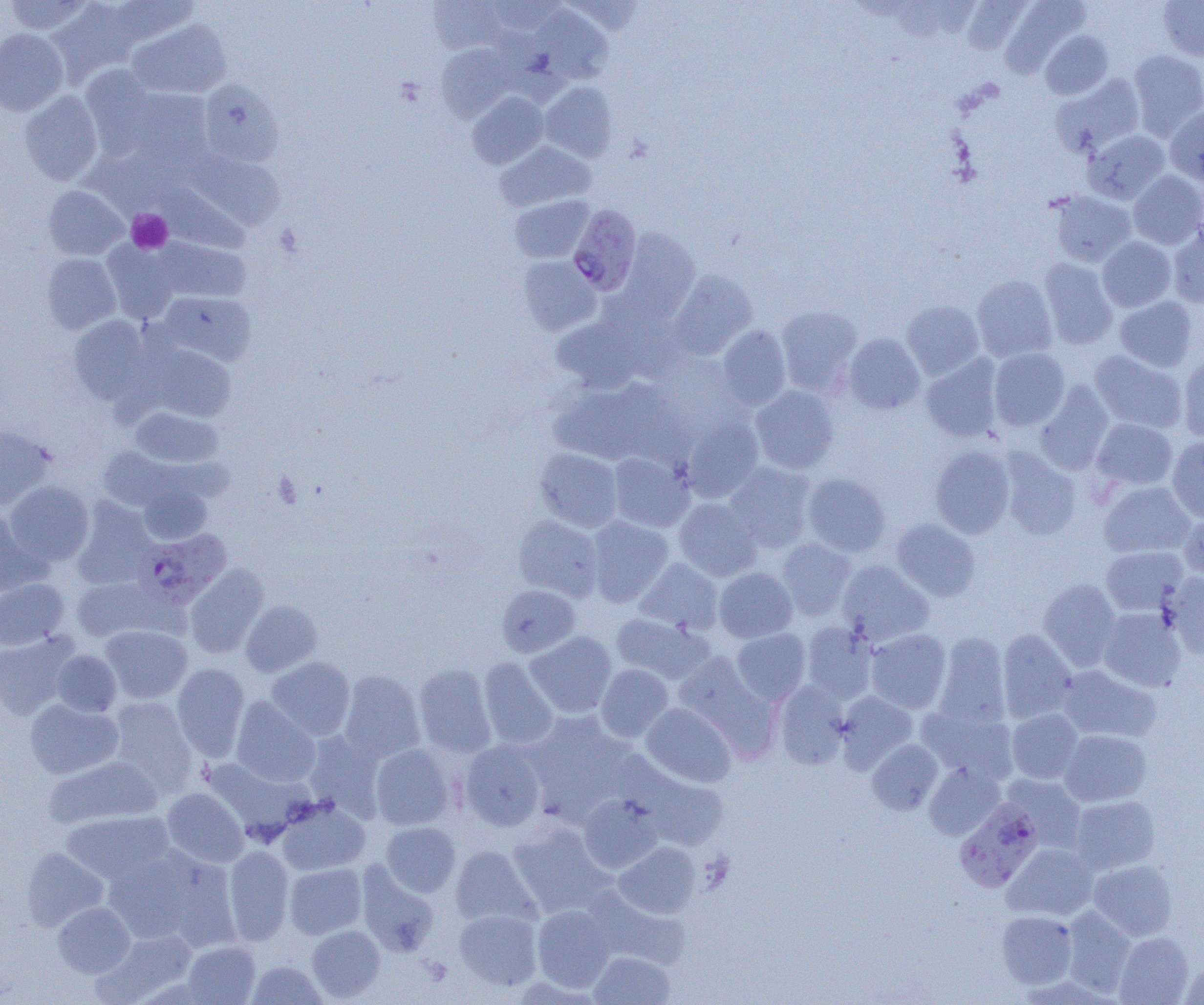
slide-level diagnosis = Plasmodium falciparum
image size = 1204×1005 pixels
platelet locations = approximate bounding boxes as (x1, y1, x2, y2) in pixels: (127, 209, 172, 253)
uninfected red blood cell locations = approximate bounding boxes as (x1, y1, x2, y2) in pixels: (3, 0, 93, 36), (108, 0, 200, 49), (428, 0, 508, 54), (484, 0, 566, 36), (960, 0, 1032, 56), (46, 1, 138, 84), (999, 1, 1090, 77), (1157, 1, 1204, 61), (531, 5, 613, 86), (126, 19, 231, 99), (0, 28, 68, 115), (1040, 31, 1114, 100), (435, 43, 515, 121), (1128, 49, 1204, 139), (81, 66, 159, 153), (1050, 74, 1145, 157), (197, 80, 284, 167), (539, 81, 618, 162), (123, 87, 215, 172), (20, 90, 103, 186), (467, 91, 548, 169), (1165, 105, 1204, 185), (1083, 129, 1170, 204), (495, 140, 595, 212), (183, 150, 285, 229), (1128, 170, 1204, 249), (159, 184, 249, 253), (43, 185, 129, 260), (1047, 190, 1136, 267), (510, 195, 594, 264), (1168, 224, 1204, 308), (612, 228, 700, 325), (152, 237, 250, 304), (1097, 237, 1176, 311), (102, 240, 180, 323), (42, 253, 122, 334), (518, 255, 601, 336), (1039, 258, 1118, 350), (666, 270, 757, 360), (972, 275, 1057, 362), (156, 291, 257, 367), (1115, 296, 1199, 372), (900, 299, 984, 380), (777, 305, 862, 395), (68, 315, 155, 405), (552, 317, 644, 393), (716, 325, 791, 411), (842, 333, 925, 415), (145, 345, 236, 422), (989, 348, 1070, 431), (1089, 350, 1187, 433), (1178, 353, 1204, 444), (920, 354, 1003, 442), (548, 379, 663, 466), (1033, 381, 1114, 475), (750, 386, 839, 475), (130, 406, 223, 468), (681, 415, 763, 502), (1091, 418, 1178, 492), (0, 424, 55, 509), (1167, 437, 1204, 521), (929, 445, 1015, 538), (97, 447, 181, 512), (534, 448, 622, 532), (998, 449, 1081, 540), (607, 452, 694, 532), (723, 463, 816, 553), (802, 472, 891, 557), (5, 480, 94, 566), (1099, 481, 1195, 558), (138, 483, 212, 546), (72, 498, 157, 588), (673, 498, 761, 581), (0, 508, 44, 597), (1178, 512, 1204, 582), (513, 514, 604, 601), (586, 515, 673, 607), (891, 518, 981, 602), (776, 538, 857, 620), (1101, 546, 1188, 615), (635, 558, 723, 634), (837, 560, 934, 646), (183, 565, 269, 658), (714, 567, 798, 643), (1163, 573, 1204, 660), (69, 575, 167, 643), (0, 578, 69, 650), (1038, 578, 1121, 671), (496, 585, 580, 658), (241, 600, 322, 677), (1098, 607, 1186, 692), (611, 613, 714, 684), (801, 621, 877, 703), (100, 625, 192, 704), (865, 628, 951, 713), (731, 629, 811, 704), (997, 629, 1077, 723), (0, 631, 78, 719), (525, 631, 617, 719), (934, 633, 1011, 726), (51, 649, 122, 717), (673, 652, 776, 753), (478, 656, 558, 750), (266, 657, 355, 741), (172, 663, 250, 762), (413, 663, 497, 758), (595, 664, 673, 743), (1057, 665, 1161, 743), (339, 669, 425, 762), (773, 680, 849, 769), (835, 691, 917, 773), (105, 696, 198, 796), (230, 696, 320, 787), (24, 698, 123, 779), (640, 702, 737, 788), (917, 703, 1018, 785), (1007, 709, 1084, 784), (525, 711, 637, 822), (1059, 729, 1152, 806), (302, 730, 386, 821), (459, 739, 547, 831), (867, 739, 943, 815), (370, 743, 457, 830), (610, 749, 731, 850), (43, 754, 162, 831), (202, 757, 312, 841), (924, 762, 1005, 840), (1001, 774, 1087, 852), (162, 788, 248, 867), (578, 793, 664, 873), (1069, 795, 1160, 875), (277, 798, 370, 876), (59, 810, 174, 885), (507, 821, 615, 918), (380, 822, 460, 896), (614, 842, 700, 918), (1003, 843, 1098, 921), (103, 845, 222, 946), (223, 845, 294, 945), (450, 845, 541, 929), (22, 847, 108, 931), (1088, 859, 1178, 941), (357, 862, 440, 957), (284, 863, 367, 939), (583, 886, 689, 970), (52, 901, 135, 978), (531, 905, 616, 992), (1060, 906, 1136, 996), (454, 909, 542, 991), (996, 910, 1078, 989), (306, 925, 385, 1002), (96, 929, 197, 1002), (1115, 932, 1194, 1005), (182, 941, 260, 1004), (589, 951, 675, 1004), (247, 960, 326, 1005), (1179, 962, 1204, 1004)
preparation = thin blood smear
field of view = single
magnification = 1000x
Plasmodium falciparum-infected red blood cell locations = approximate bounding boxes as (x1, y1, x2, y2) in pixels: (567, 204, 642, 296), (133, 528, 233, 609), (954, 798, 1044, 892)
modality = optical microscopy